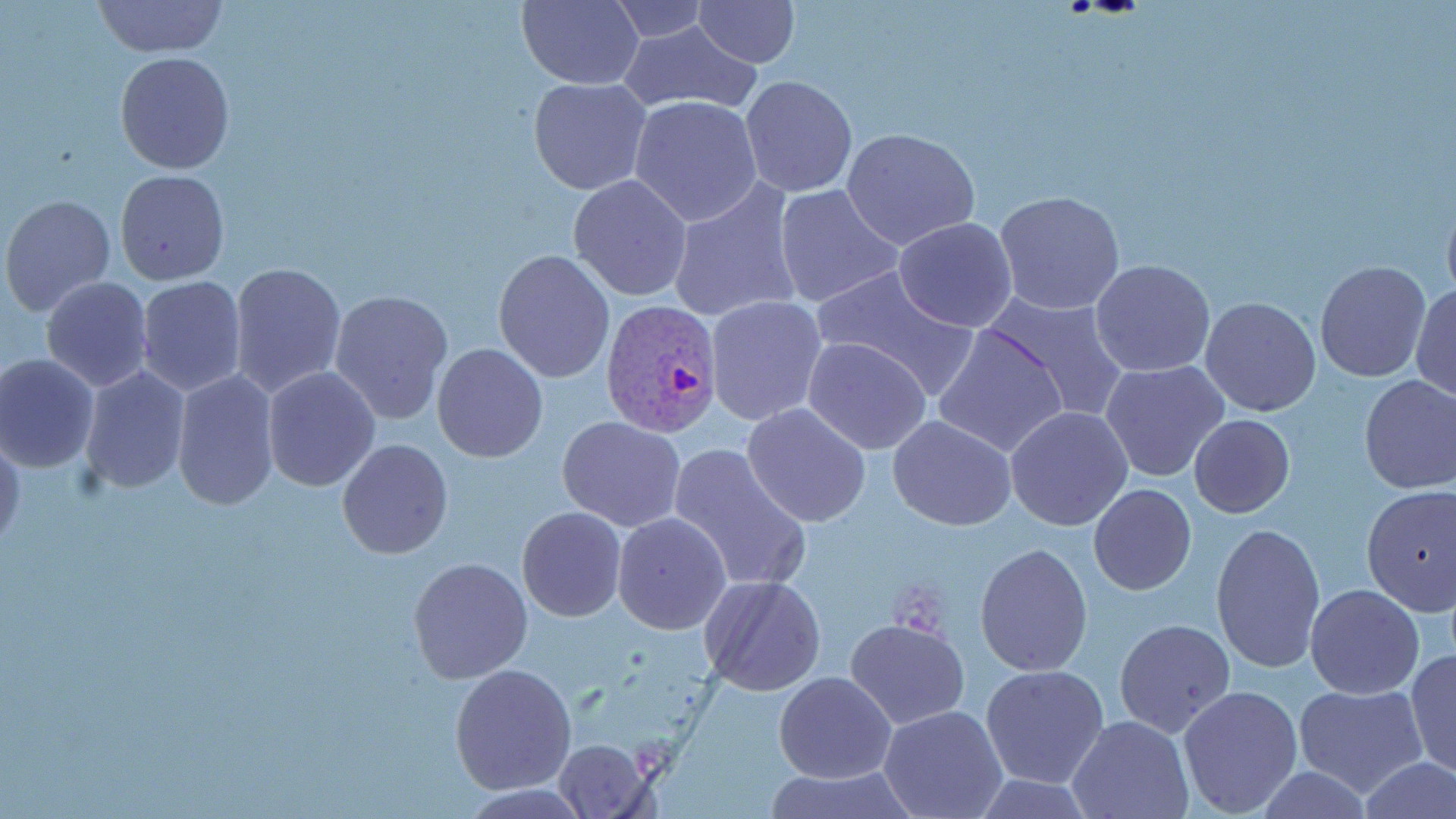

slide-level diagnosis = Plasmodium vivax
field of view = one of a larger specimen
uninfected red blood cell locations = approximate bounding boxes as (x1,y1)-(x2,y2) corner pairs in pixels: (91,0)-(226,57), (516,0)-(643,90), (691,0)-(799,67), (610,2)-(708,42), (616,20)-(760,116), (114,51)-(234,174), (740,75)-(857,197), (528,77)-(654,195), (629,95)-(763,227), (841,127)-(980,251), (114,169)-(231,287), (567,174)-(693,302), (665,176)-(804,325), (773,185)-(903,309), (2,186)-(227,302), (1441,188)-(1456,309), (994,191)-(1126,317), (2,195)-(117,319), (892,217)-(1018,333), (493,248)-(615,382), (1090,258)-(1214,378), (227,261)-(346,398), (1314,261)-(1432,383), (812,265)-(982,399), (135,275)-(248,398), (40,278)-(154,392), (1411,283)-(1455,403), (329,289)-(455,426), (982,291)-(1132,423), (706,296)-(829,429), (1200,296)-(1322,417), (933,322)-(1071,459), (802,337)-(933,455), (431,343)-(549,463), (0,352)-(100,473), (1100,359)-(1229,483), (79,366)-(192,497), (170,367)-(281,511), (261,367)-(381,493), (1357,373)-(1456,494), (741,403)-(871,529), (1005,406)-(1134,531), (1189,414)-(1295,518), (558,416)-(686,532), (888,416)-(1017,531), (0,434)-(25,555), (337,438)-(452,558), (665,443)-(811,594), (1088,484)-(1197,596), (1360,485)-(1456,615), (517,506)-(627,621), (613,512)-(732,635), (1209,522)-(1325,676), (973,542)-(1094,678), (407,556)-(531,684), (698,576)-(826,696), (1305,583)-(1426,700), (844,617)-(970,730), (1113,618)-(1236,737), (1405,649)-(1455,777), (450,663)-(578,796), (980,664)-(1108,787), (773,672)-(895,783), (1177,683)-(1304,819), (1292,683)-(1428,798), (878,706)-(1007,819), (1067,715)-(1194,819), (550,737)-(655,817), (1357,758)-(1454,818), (762,766)-(921,819)
Plasmodium vivax-infected red blood cell locations = approximate bounding boxes as (x1,y1)-(x2,y2) corner pairs in pixels: (600,299)-(725,437)
modality = optical microscopy
magnification = 1000x
preparation = thin blood smear
stain = May-Grünwald-Giemsa
image size = 1456×819 pixels